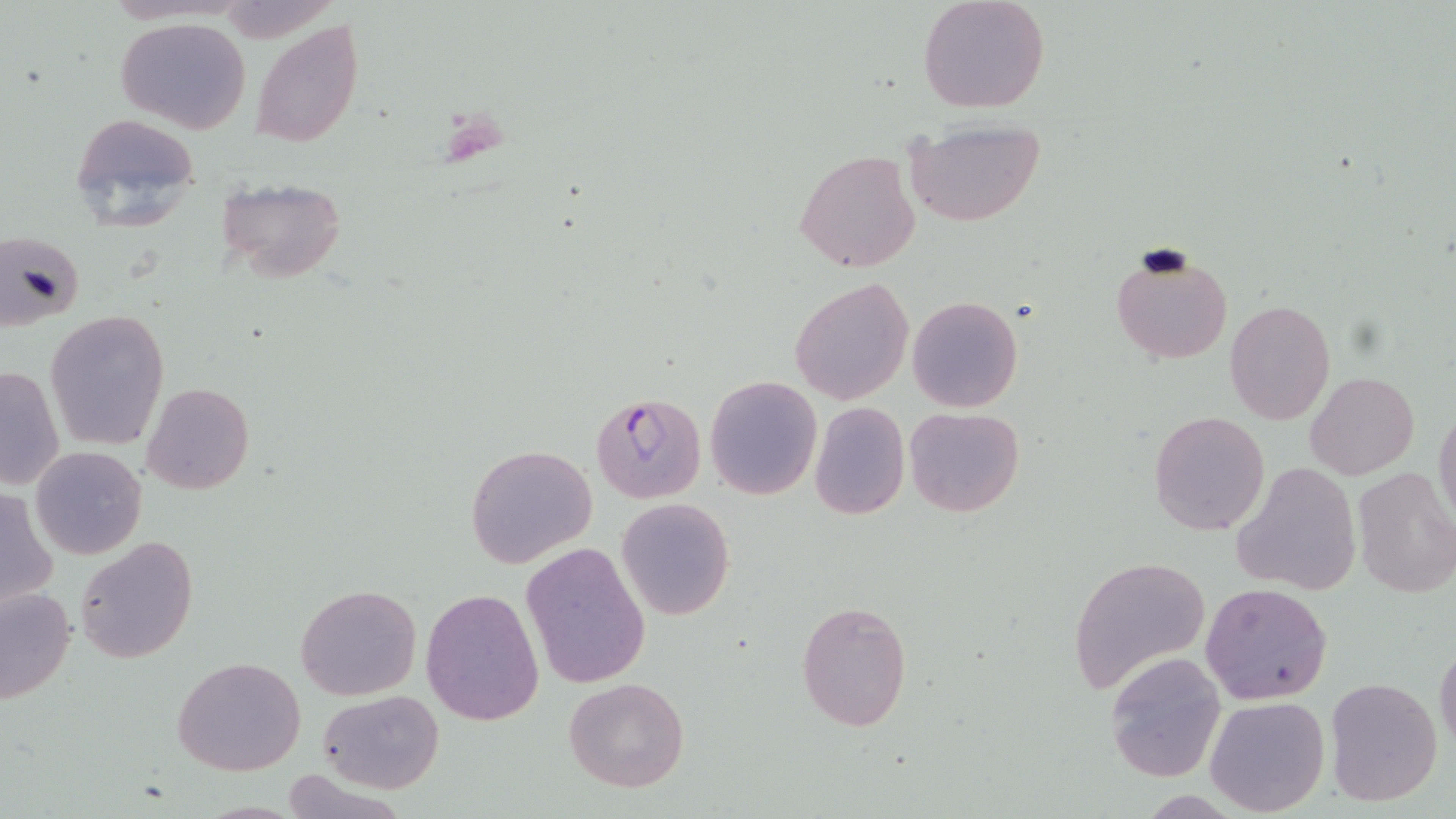
slide-level diagnosis = Plasmodium falciparum
modality = optical microscopy
Plasmodium falciparum-infected red blood cell locations = approximate bounding boxes as named x1/y1/x2/y2 corners in pixels: (x1=591, y1=392, x2=707, y2=503)
uninfected red blood cell locations = approximate bounding boxes as named x1/y1/x2/y2 corners in pixels: (x1=918, y1=0, x2=1051, y2=115), (x1=115, y1=17, x2=252, y2=133), (x1=251, y1=19, x2=365, y2=148), (x1=67, y1=112, x2=199, y2=234), (x1=903, y1=119, x2=1047, y2=226), (x1=794, y1=149, x2=922, y2=273), (x1=215, y1=176, x2=347, y2=283), (x1=2, y1=231, x2=85, y2=331), (x1=1109, y1=244, x2=1235, y2=367), (x1=790, y1=277, x2=914, y2=404), (x1=907, y1=296, x2=1023, y2=413), (x1=1225, y1=300, x2=1336, y2=423), (x1=45, y1=310, x2=168, y2=450), (x1=1, y1=364, x2=66, y2=492), (x1=1305, y1=371, x2=1418, y2=479), (x1=704, y1=374, x2=822, y2=501), (x1=142, y1=383, x2=255, y2=495), (x1=809, y1=402, x2=910, y2=519), (x1=1433, y1=403, x2=1456, y2=532), (x1=906, y1=407, x2=1024, y2=517), (x1=1149, y1=411, x2=1270, y2=535), (x1=466, y1=443, x2=597, y2=571), (x1=29, y1=446, x2=147, y2=560), (x1=1234, y1=463, x2=1362, y2=597), (x1=1352, y1=465, x2=1456, y2=598), (x1=0, y1=488, x2=57, y2=610), (x1=617, y1=497, x2=734, y2=620), (x1=75, y1=536, x2=198, y2=663), (x1=519, y1=542, x2=652, y2=690), (x1=1067, y1=555, x2=1211, y2=696), (x1=1201, y1=581, x2=1332, y2=704), (x1=294, y1=583, x2=421, y2=701), (x1=1, y1=585, x2=76, y2=706), (x1=421, y1=587, x2=544, y2=725), (x1=796, y1=600, x2=912, y2=731), (x1=1434, y1=639, x2=1456, y2=757), (x1=1104, y1=652, x2=1228, y2=783), (x1=172, y1=655, x2=306, y2=776), (x1=1323, y1=676, x2=1444, y2=807), (x1=562, y1=677, x2=691, y2=791), (x1=317, y1=688, x2=443, y2=793), (x1=1205, y1=695, x2=1329, y2=817)
field of view = single
stain = May-Grünwald-Giemsa
image size = 1456×819 pixels
preparation = thin blood smear
magnification = 1000x